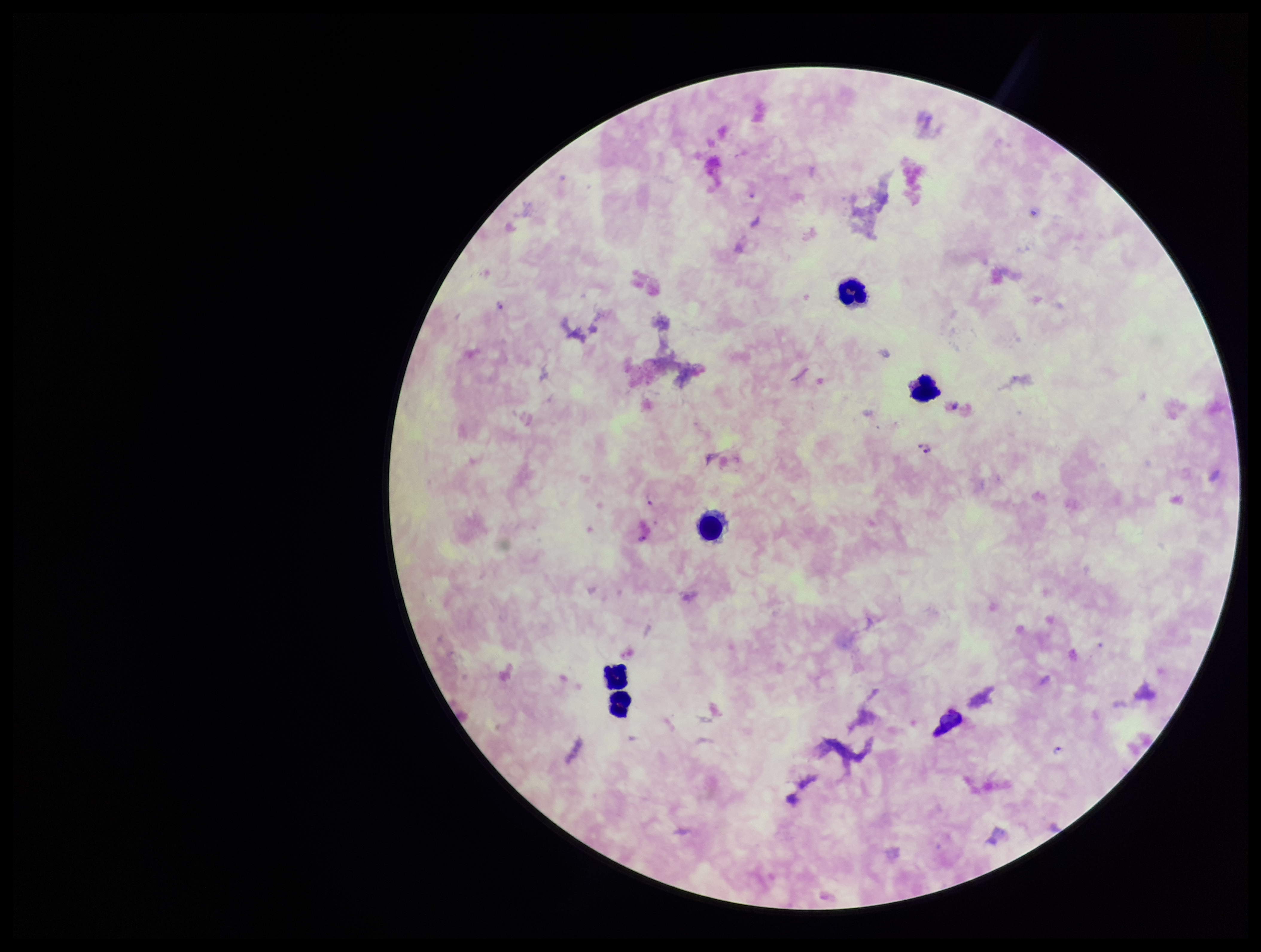
Summary:
  - Image size: 1261×952 pixels
  - Preparation: thick
  - Parasite count: 3
  - Stain: Giemsa
  - Leukocyte count: 5
  - Plasmodium parasites: detected
  - Patient malaria status: positive
  - Species reported for this patient: Plasmodium falciparum
  - Capture: smartphone photograph through the microscope eyepiece
  - Field of view: single